Assess this cell for malaria.
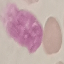
It is uninfected.

Summary:
  - Preparation: thin blood film
  - Stain: Giemsa
  - Capture: smartphone camera at the microscope eyepiece
  - Image type: cell patch, automatically extracted from a larger field of view and resized to 64 × 64 pixels